Report the malaria status of this cell.
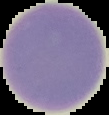
It is uninfected.

Summary:
  - Image size: 109×115 pixels
  - Preparation: thin blood film
  - Image type: cell region segmented out of the field of view; surrounding area masked to black